Name the parasite shown.
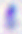

This is Toxoplasma gondii.

modality = photomicrograph
magnification = 400x